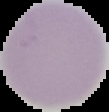

Summary:
  - Image type: cell region segmented out of the field of view; surrounding area masked to black
  - Preparation: thin blood film
  - Malaria status: uninfected
  - Image size: 109×112 pixels